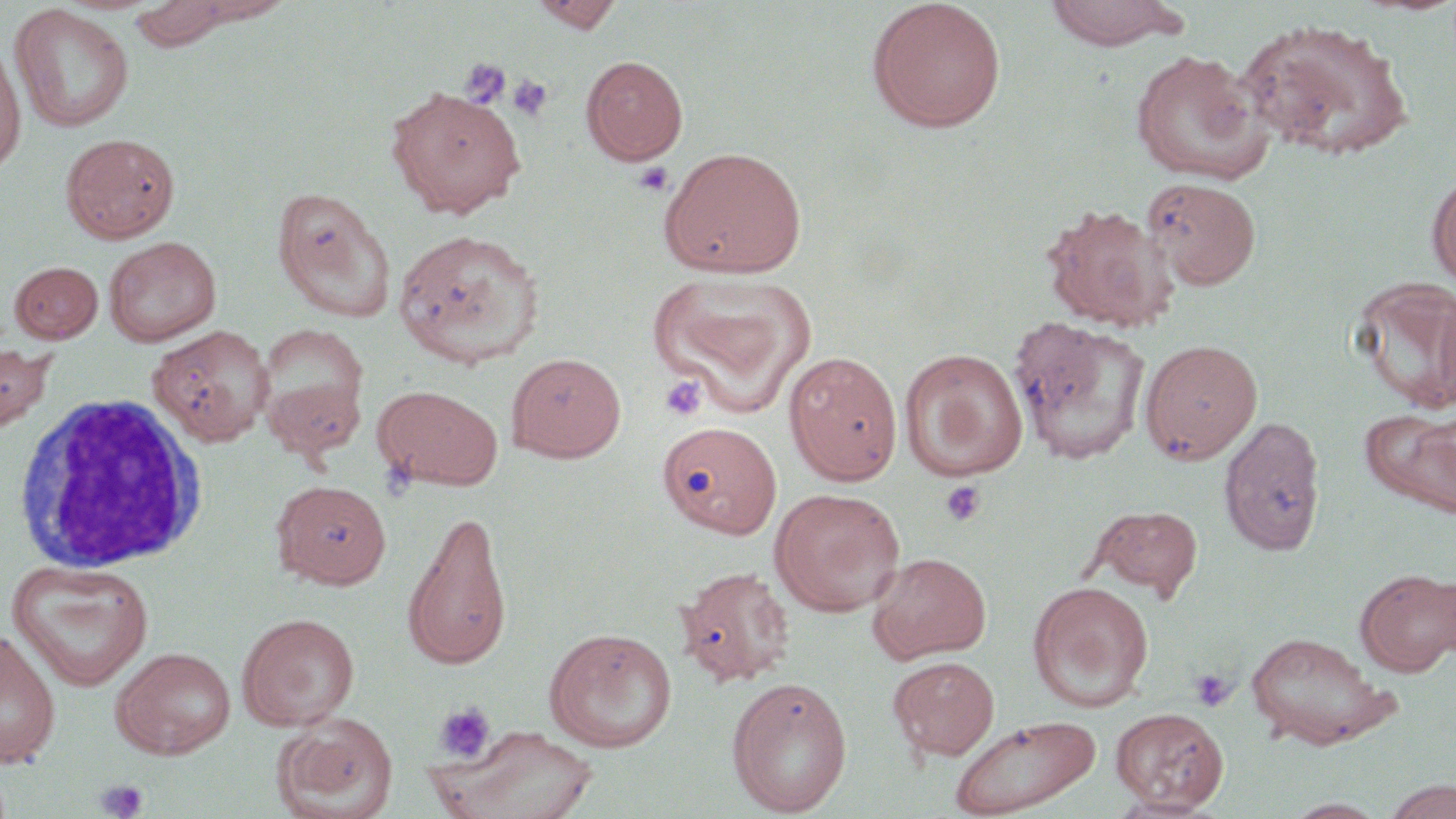

{
  "slide_level_diagnosis": "no evidence of blood parasites",
  "platelet_locations": "approximate bounding boxes as (x1, y1, x2, y2) in pixels: (459, 58, 510, 109), (506, 75, 553, 122), (632, 161, 675, 197), (659, 374, 708, 422), (941, 480, 986, 527), (1188, 668, 1237, 713), (434, 702, 496, 763), (94, 778, 149, 819)",
  "uninfected_red_blood_cell_locations": "approximate bounding boxes as (x1, y1, x2, y2) in pixels: (182, 0, 296, 26), (865, 0, 1007, 133), (1042, 0, 1188, 52), (128, 1, 234, 52), (528, 1, 624, 33), (9, 4, 135, 133), (1236, 17, 1415, 162), (0, 42, 26, 178), (1130, 49, 1274, 184), (580, 55, 688, 165), (385, 85, 525, 217), (60, 132, 180, 244), (659, 146, 807, 279), (1426, 170, 1456, 292), (1143, 177, 1261, 290), (271, 186, 396, 322), (1040, 203, 1178, 331), (392, 228, 545, 368), (103, 236, 222, 346), (9, 261, 104, 343), (647, 272, 817, 415), (1351, 276, 1456, 415), (1009, 318, 1151, 465), (148, 324, 274, 447), (256, 327, 369, 454), (1139, 338, 1263, 465), (0, 340, 55, 435), (899, 348, 1029, 480), (784, 350, 903, 485), (506, 352, 626, 463), (372, 384, 503, 492), (1363, 406, 1456, 516), (1218, 414, 1327, 556), (658, 420, 781, 539), (272, 479, 392, 588), (769, 487, 906, 616), (1087, 504, 1203, 599), (402, 508, 513, 671), (867, 551, 992, 663), (6, 559, 155, 691), (675, 564, 796, 687), (1355, 567, 1455, 676), (1027, 580, 1154, 711), (236, 612, 360, 731), (543, 627, 678, 753), (0, 629, 61, 769), (1244, 631, 1395, 749), (110, 646, 237, 759), (887, 655, 1001, 761), (727, 676, 853, 816), (1111, 707, 1229, 812), (273, 713, 399, 819), (948, 714, 1101, 818), (437, 725, 600, 819), (1381, 779, 1455, 819), (1105, 794, 1223, 818), (1281, 797, 1392, 818)",
  "magnification": "1000x",
  "preparation": "thin blood film",
  "image_size": "1456×819 pixels",
  "modality": "optical microscopy",
  "stain": "May-Grünwald-Giemsa",
  "field_of_view": "single",
  "white_blood_cell_locations": "approximate bounding boxes as (x1, y1, x2, y2) in pixels: (11, 390, 210, 574)"
}